Locate every blood parasite and identify its species.
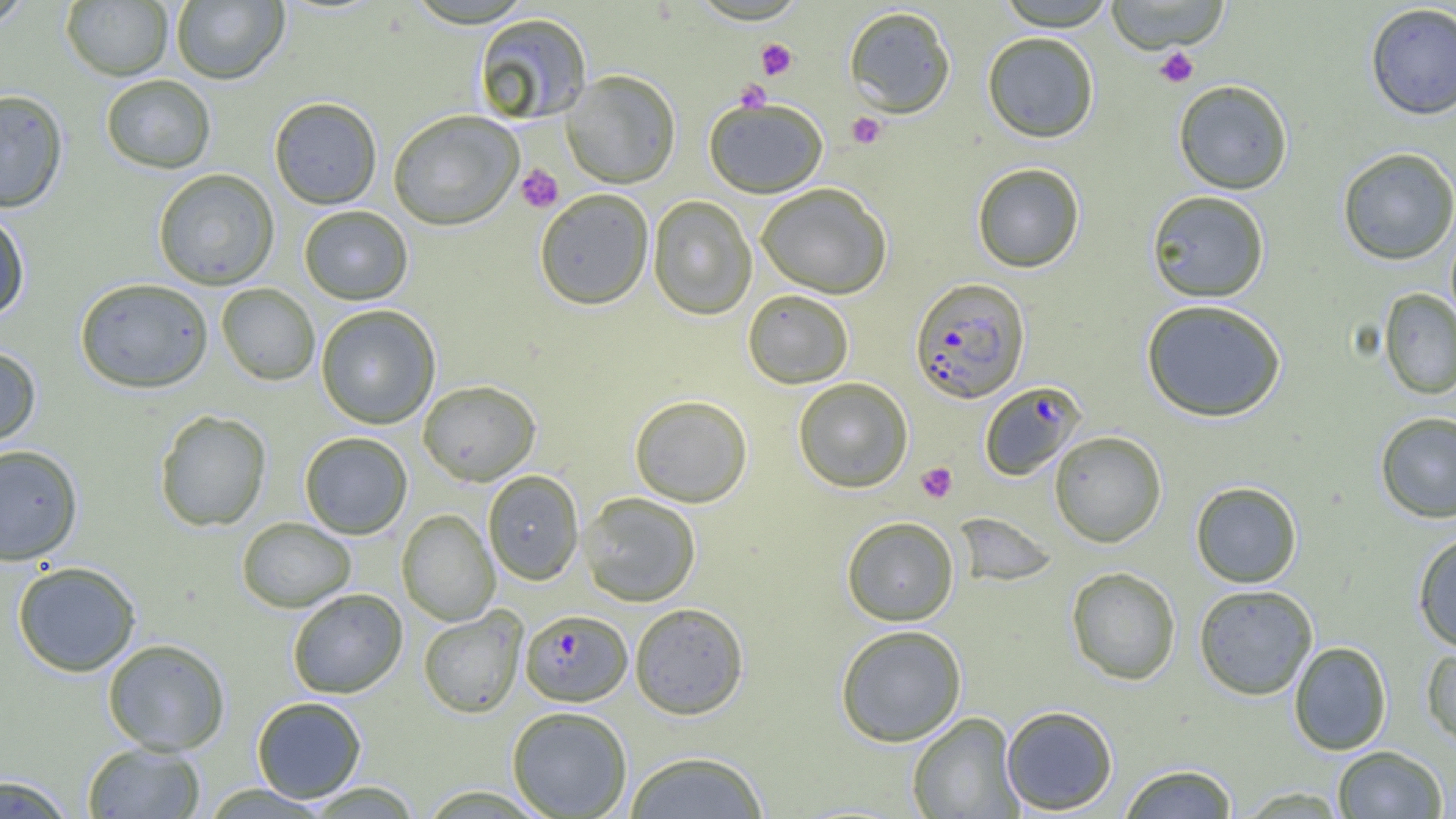
Approximate bounding boxes as (x1, y1, x2, y2) in pixels.
Plasmodium falciparum-infected red blood cells: (909, 278, 1030, 404), (979, 382, 1086, 481), (520, 610, 632, 706).
No Plasmodium ovale, Plasmodium malariae, Plasmodium vivax, Babesia divergens, or Trypanosoma brucei observed.

Uninfected red blood cell locations: (0, 0, 35, 32), (171, 0, 289, 86), (995, 0, 1117, 31), (1105, 0, 1231, 53), (61, 1, 173, 81), (1365, 3, 1456, 120), (843, 5, 956, 118), (473, 13, 592, 126), (982, 32, 1100, 143), (562, 71, 681, 189), (101, 75, 216, 174), (1173, 80, 1293, 195), (0, 89, 69, 213), (269, 97, 382, 210), (704, 98, 828, 199), (388, 111, 524, 232), (1336, 147, 1456, 266), (972, 162, 1085, 273), (153, 169, 280, 290), (756, 183, 892, 299), (534, 189, 654, 311), (1146, 190, 1270, 303), (648, 196, 756, 320), (299, 206, 413, 306), (0, 209, 30, 322), (74, 278, 213, 395), (216, 283, 320, 386), (1378, 288, 1456, 399), (742, 290, 854, 389), (1141, 299, 1287, 423), (315, 305, 440, 430), (0, 345, 42, 450), (793, 378, 913, 492), (418, 380, 541, 486), (629, 395, 753, 508), (154, 409, 272, 532), (1375, 412, 1456, 523), (1049, 431, 1167, 547), (299, 432, 412, 539), (0, 444, 83, 566), (483, 470, 584, 585), (1190, 481, 1302, 587), (579, 493, 701, 607), (396, 510, 500, 626), (953, 512, 1057, 587), (841, 516, 959, 627), (236, 517, 356, 613), (1412, 532, 1456, 653), (12, 561, 141, 677), (1066, 566, 1181, 685), (1193, 584, 1318, 700), (287, 588, 408, 699), (630, 602, 748, 720), (418, 608, 527, 718), (834, 625, 967, 747), (102, 639, 230, 756), (1288, 641, 1392, 755), (1421, 643, 1456, 749), (252, 696, 367, 802), (1001, 705, 1119, 815), (506, 706, 632, 818), (906, 712, 1023, 818), (82, 743, 206, 818), (1332, 745, 1448, 818), (622, 751, 770, 818), (1118, 763, 1238, 819), (0, 773, 76, 818), (301, 781, 424, 818), (200, 784, 333, 818), (416, 785, 552, 818), (1234, 786, 1351, 817). Platelet locations: (756, 39, 798, 80), (1154, 46, 1199, 87), (735, 80, 771, 113), (846, 112, 886, 149), (516, 164, 563, 212), (916, 462, 958, 503). Slide-level diagnosis: Plasmodium falciparum. 1000x magnification. One field of a larger specimen. Optical microscopy. Image is 1456×819 pixels. Thin blood smear.